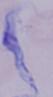

Micrograph. A trypanosome is seen. Captured at 1000x magnification.